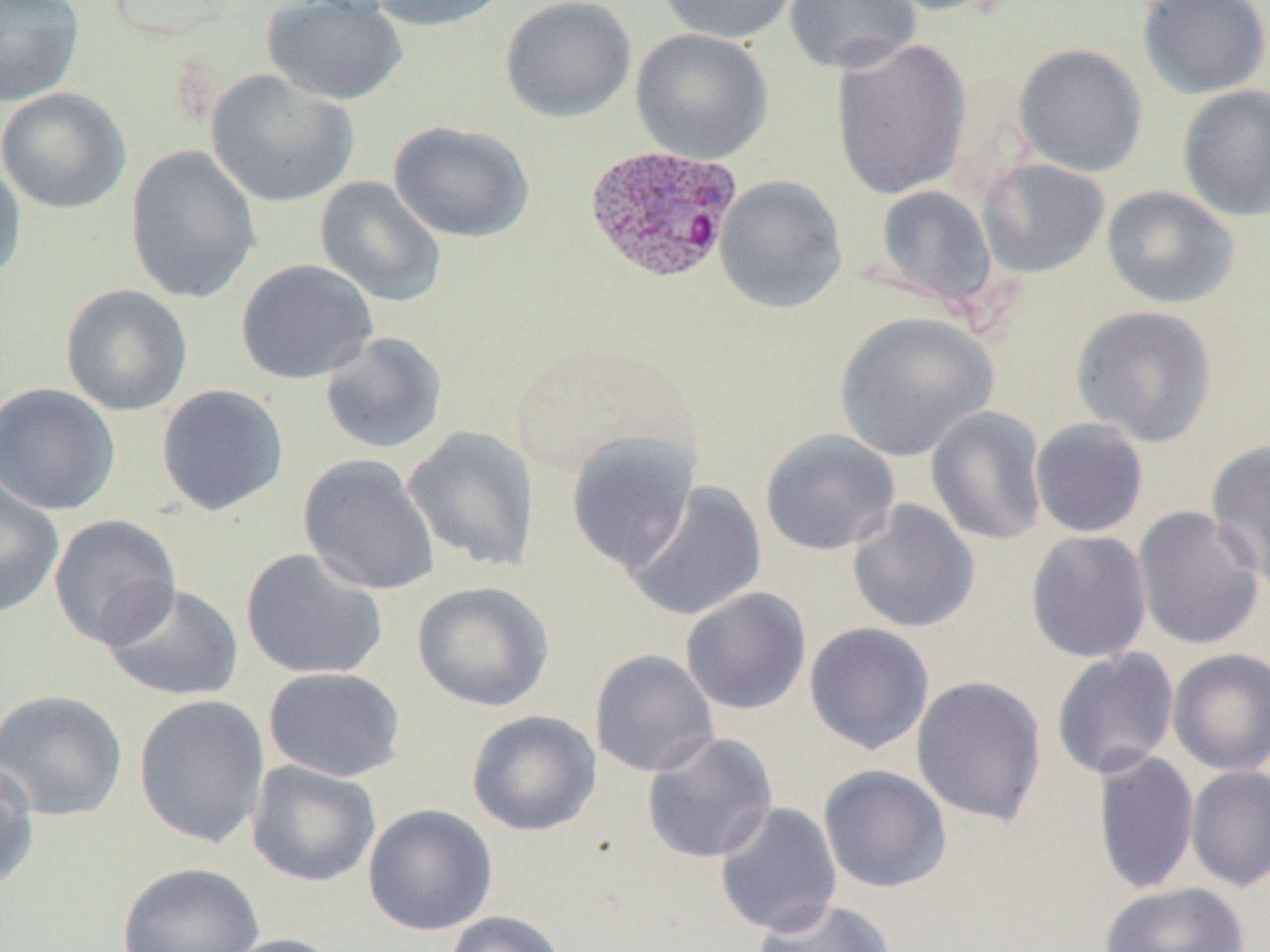
Summary:
  - Coordinate format: approximate bounding boxes as (x1, y1, x2, y2) in pixels
  - Uninfected red blood cell locations: (0, 0, 85, 107), (261, 0, 409, 106), (367, 0, 511, 32), (500, 0, 636, 123), (654, 0, 799, 44), (783, 0, 921, 74), (875, 0, 1009, 16), (1135, 0, 1270, 99), (630, 28, 774, 165), (829, 37, 973, 200), (1014, 43, 1148, 177), (206, 69, 359, 208), (1177, 84, 1270, 222), (1, 87, 132, 215), (389, 120, 535, 244), (125, 144, 262, 304), (0, 154, 26, 288), (977, 158, 1110, 278), (714, 174, 848, 314), (314, 176, 447, 309), (873, 184, 998, 311), (1101, 185, 1240, 309), (235, 259, 379, 385), (60, 284, 193, 417), (1071, 305, 1218, 448), (833, 311, 999, 462), (319, 331, 448, 455), (0, 382, 121, 516), (156, 384, 289, 517), (925, 406, 1049, 546), (1029, 418, 1149, 538), (402, 425, 540, 573), (759, 428, 901, 557), (565, 432, 700, 575), (1205, 439, 1270, 590), (298, 454, 440, 596), (0, 476, 65, 618), (623, 481, 769, 621), (847, 499, 981, 634), (1133, 505, 1266, 651), (48, 514, 182, 649), (1026, 529, 1152, 663), (240, 547, 388, 681), (99, 580, 244, 702), (411, 580, 555, 712), (680, 587, 811, 716), (804, 622, 935, 754), (1051, 648, 1180, 781), (1167, 648, 1270, 776), (589, 649, 719, 778), (263, 667, 407, 782), (911, 675, 1047, 826), (0, 689, 128, 822), (133, 694, 269, 849), (466, 710, 602, 836), (641, 731, 778, 864), (1093, 750, 1199, 896), (0, 752, 40, 895), (246, 760, 381, 888), (818, 765, 952, 893), (1186, 765, 1270, 893), (714, 802, 842, 937), (363, 803, 498, 936), (117, 861, 265, 952), (1099, 882, 1250, 952), (752, 896, 898, 952), (443, 910, 569, 952), (220, 932, 353, 952)
  - Plasmodium ovale-infected red blood cell locations: (584, 144, 743, 285)
  - Slide-level diagnosis: Plasmodium ovale
  - Stain: May-Grünwald-Giemsa
  - Modality: optical microscopy
  - Preparation: thin blood smear
  - Field of view: single
  - Magnification: 1000x
  - Image size: 1270×952 pixels